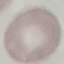

Malaria status: uninfected. Automatically extracted cell patch, resized to 64 × 64 pixels. Thin blood film. Giemsa-stained preparation. Photographed with a smartphone camera at the microscope eyepiece.